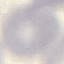
malaria status = uninfected
image type = cell patch, automatically extracted from a larger field of view and resized to 64 × 64 pixels
stain = Giemsa
capture = smartphone camera at the microscope eyepiece
preparation = thin blood film